Identify the parasite.
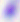
Toxoplasma gondii.

magnification: 400x
modality: micrograph